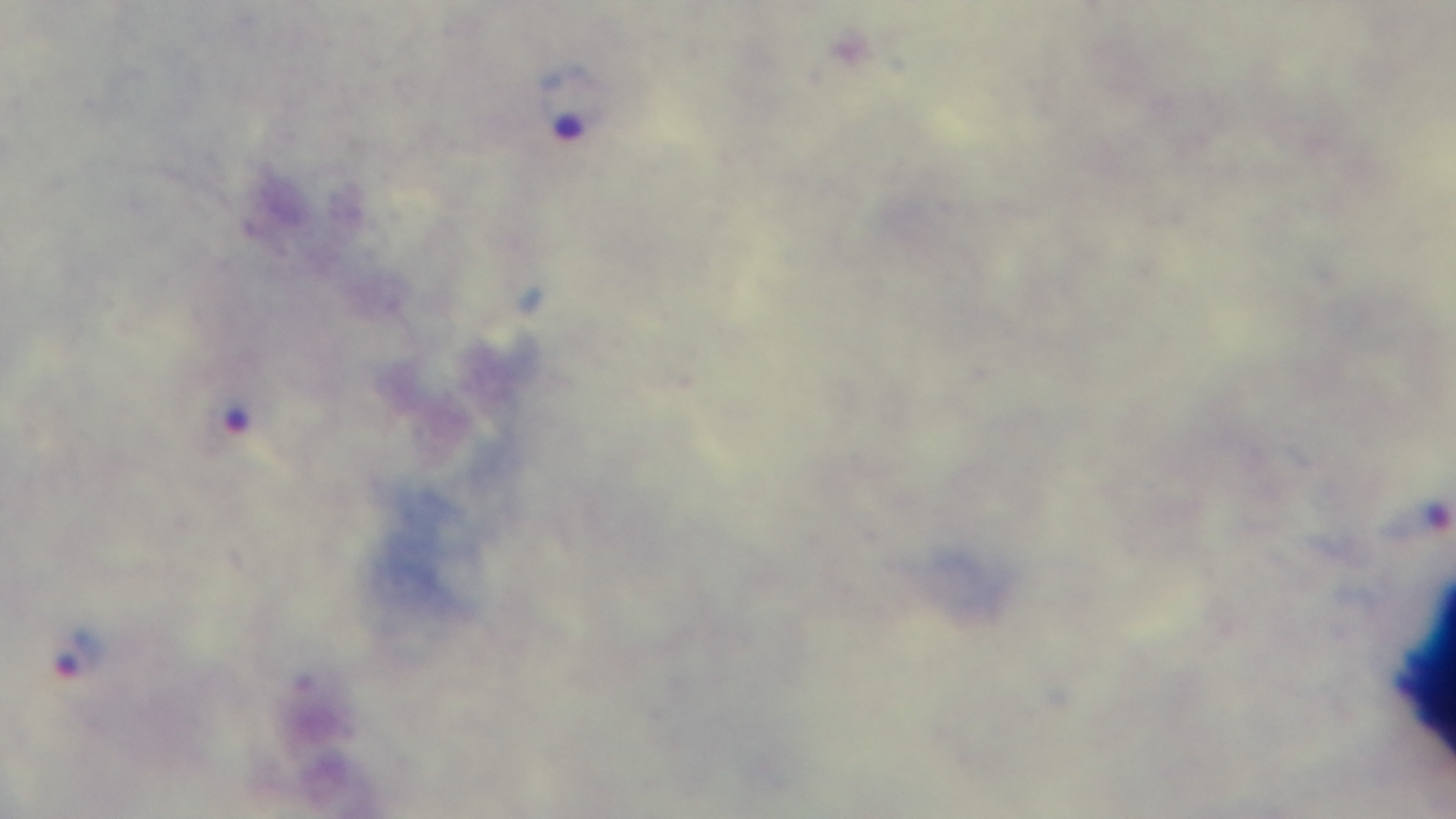
Single field of view. Preparation: thick blood film. Giemsa stain. Malaria status: infected. 100x oil-immersion objective. Mounted 4K digital camera. Light microscopy.